Report the malaria status of this cell.
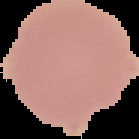
It is uninfected.

Summary:
  - Image size: 139×139 pixels
  - Image type: segmented cell region with the area outside set to black
  - Preparation: thin blood film